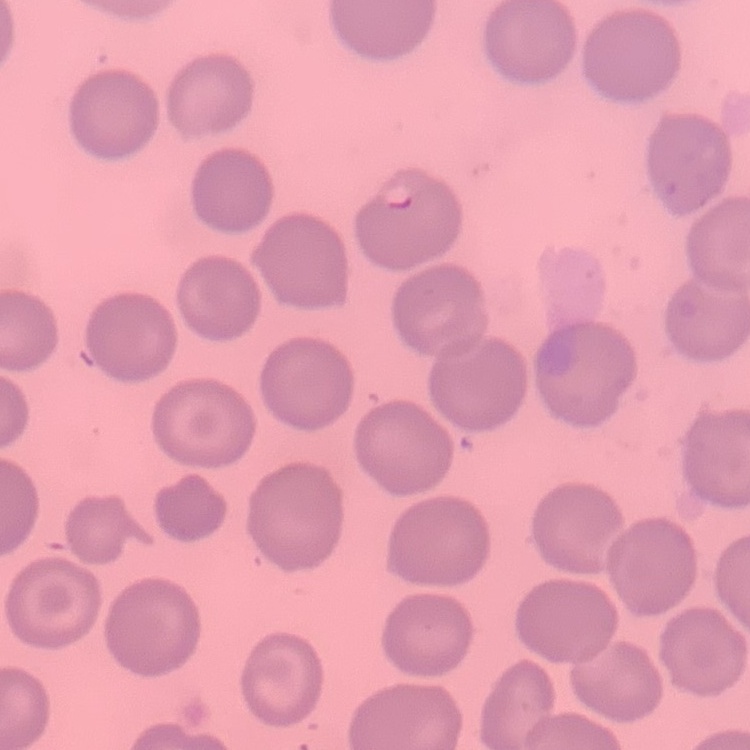 The red blood cells exhibit no rouleaux formation. One tile cut from a larger photomicrograph. Thin peripheral smear. Stained with either Field's or Giemsa.